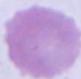

Summary:
  - Magnification: 1000x
  - Identification: erythrocyte
  - Modality: photomicrograph